Describe the morphology of the red blood cells.
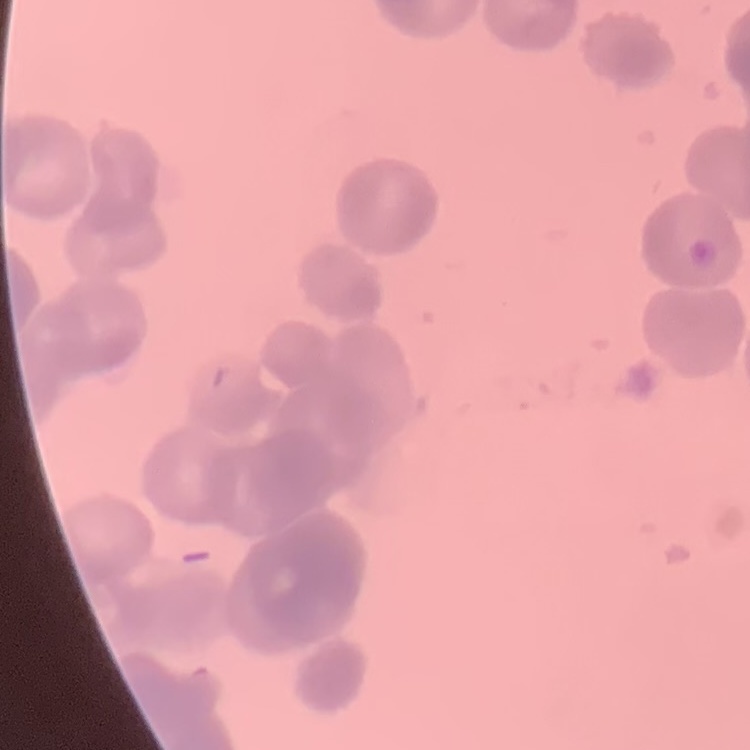

They show rouleaux formation.

Summary:
  - Preparation: thin blood film
  - Image type: one tile cut from a larger photomicrograph
  - Stain: Field's or Giemsa